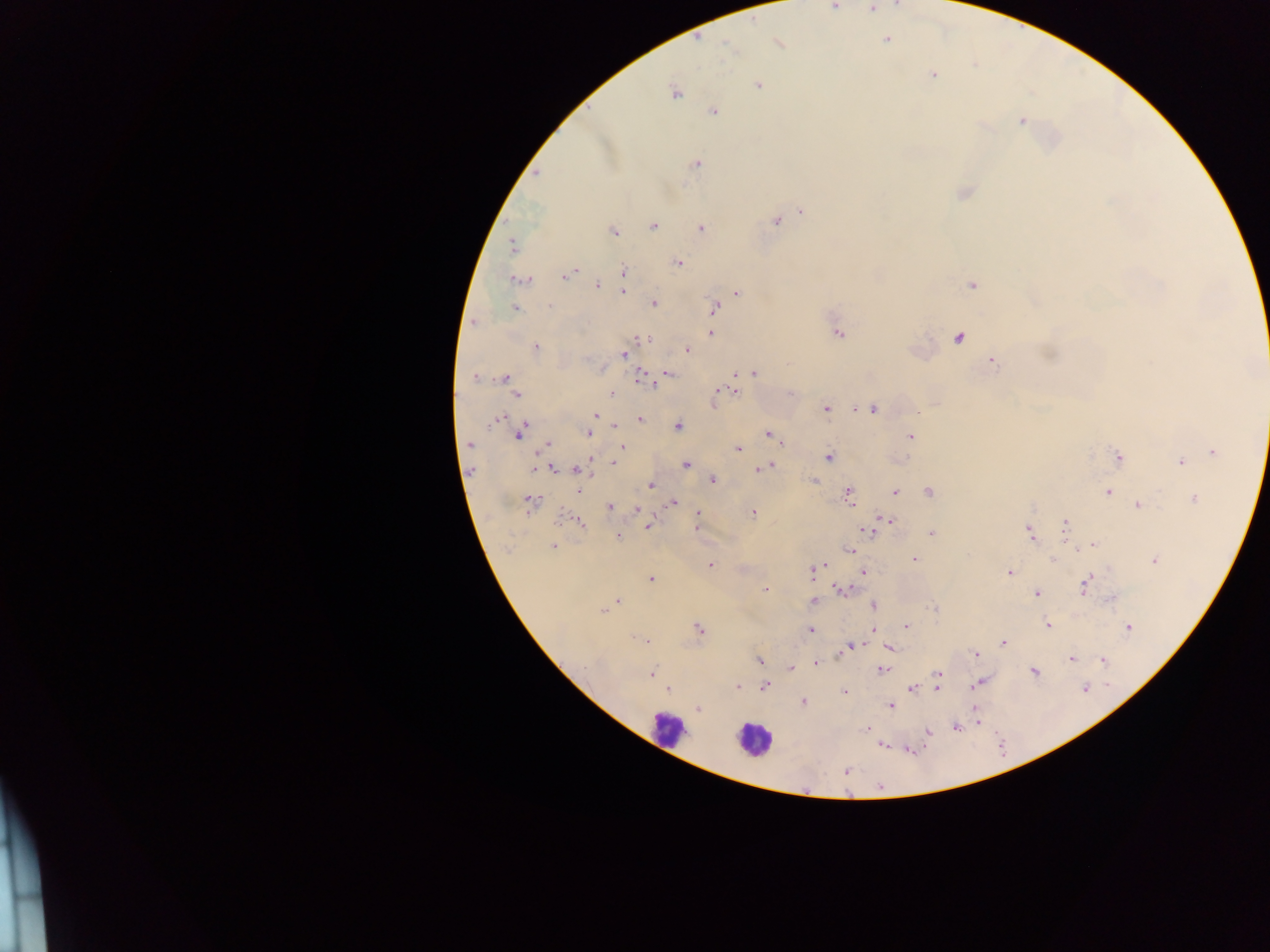
Approximate centers as x y in pixels.
Summary:
  - Malaria parasite locations: 835 6; 871 9; 886 39; 779 44; 728 46; 933 74; 758 85; 675 93; 714 111; 1022 121; 696 164; 536 173; 802 211; 776 221; 653 226; 701 228; 613 232; 512 247; 679 262; 576 271; 623 271; 567 275; 522 280; 597 286; 971 286; 623 291; 737 292; 654 303; 550 306; 514 308; 714 309; 473 323; 710 334; 838 334; 958 338; 646 339; 536 348; 686 350; 624 354; 992 362; 669 373; 753 373; 641 377; 474 378; 504 378; 652 384; 735 391; 718 392; 612 394; 790 395; 518 396; 713 404; 873 408; 826 409; 856 409; 919 413; 595 415; 497 419; 640 419; 494 422; 614 426; 678 426; 588 433; 768 433; 519 435; 910 437; 468 444; 781 444; 548 445; 622 447; 738 449; 1214 452; 1118 457; 828 458; 590 460; 614 462; 1180 462; 687 464; 771 466; 535 468; 554 469; 758 469; 578 470; 712 480; 813 480; 652 486; 579 491; 895 492; 929 492; 1108 492; 848 494; 1194 499; 531 501; 672 502; 1138 505; 610 507; 638 510; 697 513; 753 513; 888 520; 579 522; 1065 525; 647 526; 696 527; 868 530; 1029 532; 932 533; 618 536; 1092 545; 553 546; 850 549; 915 559; 1054 559; 1155 560; 711 564; 824 564; 814 570; 1009 572; 864 573; 651 579; 1085 585; 842 589; 765 590; 1037 593; 618 601; 814 602; 873 605; 934 608; 603 611; 1048 625; 907 626; 1128 627; 699 628; 873 629; 811 630; 635 639; 646 641; 1003 642; 854 646; 849 648; 890 648; 975 654; 1071 658; 759 660; 1103 660; 817 664; 790 668; 882 669; 1035 672; 652 674; 938 675; 978 683; 737 687; 765 687; 910 688; 937 688; 1084 688; 668 689; 844 692; 803 702; 890 706; 698 708; 957 727; 866 728; 928 732; 882 746; 846 770
  - Leukocyte locations: 668 730; 752 740
  - Image size: 1270×952 pixels
  - Country: Ghana
  - Capture: mobile-phone photograph through a microscope
  - Field of view: single
  - Preparation: thick blood film